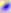
modality = photomicrograph
identification = Toxoplasma gondii
magnification = 400x